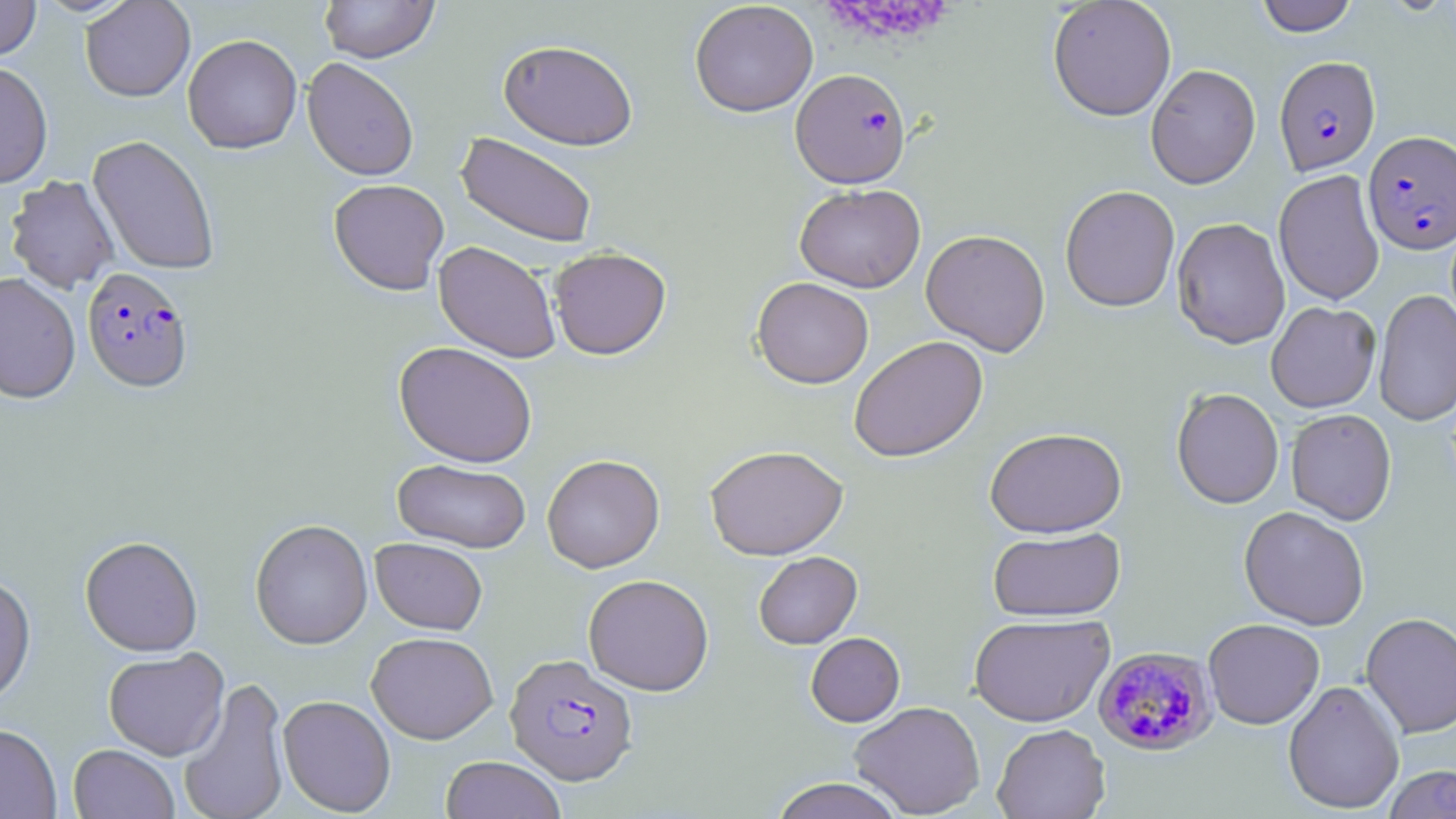
Approximate bounding boxes as [x1, y1, x2, y2] in pixels. Plasmodium falciparum-infected red blood cell locations: [1275, 55, 1380, 174], [791, 68, 911, 188], [1363, 131, 1455, 254], [82, 267, 193, 392], [1092, 645, 1219, 757], [506, 654, 638, 785]. Uninfected red blood cell locations: [0, 0, 41, 61], [80, 0, 196, 102], [319, 0, 439, 63], [1047, 0, 1177, 121], [1256, 0, 1358, 36], [689, 1, 818, 117], [182, 34, 302, 153], [498, 39, 639, 150], [302, 57, 419, 181], [0, 60, 53, 189], [1145, 63, 1261, 189], [456, 132, 598, 248], [88, 135, 221, 275], [1273, 169, 1385, 305], [6, 174, 120, 294], [328, 178, 450, 295], [794, 184, 925, 293], [1060, 184, 1180, 312], [1172, 217, 1290, 349], [921, 229, 1051, 356], [434, 241, 561, 363], [549, 246, 672, 360], [0, 273, 81, 404], [752, 277, 874, 388], [1374, 289, 1456, 428], [1265, 301, 1380, 412], [849, 336, 988, 462], [394, 341, 538, 467], [1171, 387, 1284, 509], [1286, 408, 1397, 525], [984, 427, 1127, 538], [705, 445, 848, 560], [542, 454, 665, 573], [392, 459, 531, 553], [1239, 506, 1370, 630], [250, 518, 373, 650], [988, 527, 1125, 621], [79, 535, 203, 656], [371, 537, 487, 634], [753, 551, 862, 649], [0, 572, 36, 707], [583, 574, 714, 696], [1361, 611, 1456, 739], [968, 613, 1114, 727], [1203, 618, 1325, 729], [366, 631, 498, 744], [806, 632, 905, 726], [103, 648, 229, 760], [178, 676, 290, 819], [1283, 679, 1405, 814], [277, 694, 396, 816], [850, 700, 985, 817], [0, 723, 62, 818], [992, 723, 1110, 818], [68, 743, 180, 819], [440, 755, 567, 819], [1383, 765, 1456, 818], [769, 777, 905, 819]. Slide-level diagnosis: Plasmodium falciparum. Thin blood smear. Image is 1456×819 pixels. Optical microscopy. May-Grünwald-Giemsa-stained preparation. 1000x magnification. One field of a larger specimen.